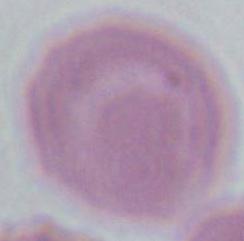
modality = micrograph
identification = red blood cell
magnification = 1000x